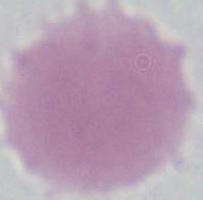

Summary:
  - Identification: erythrocyte
  - Modality: micrograph
  - Magnification: 1000x